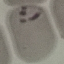 Malaria status: parasitized. Giemsa-stained preparation. Cell patch, automatically extracted from a larger field of view and resized to 64 × 64 pixels. Thin blood film. Photographed with a smartphone camera at the microscope eyepiece.